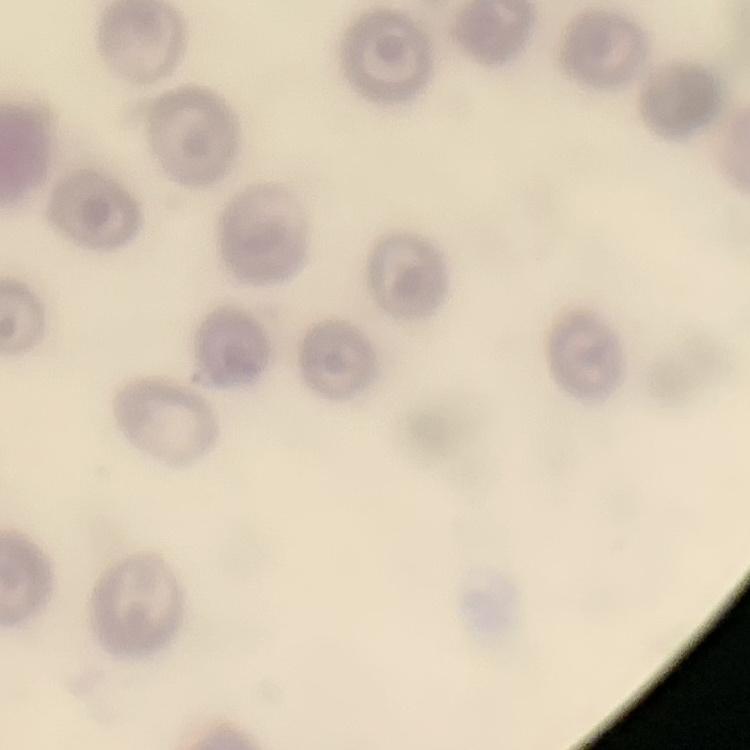
The red blood cells show no rouleaux formation. Thin blood smear. One tile cut from a larger photomicrograph. Field's or Giemsa stain.